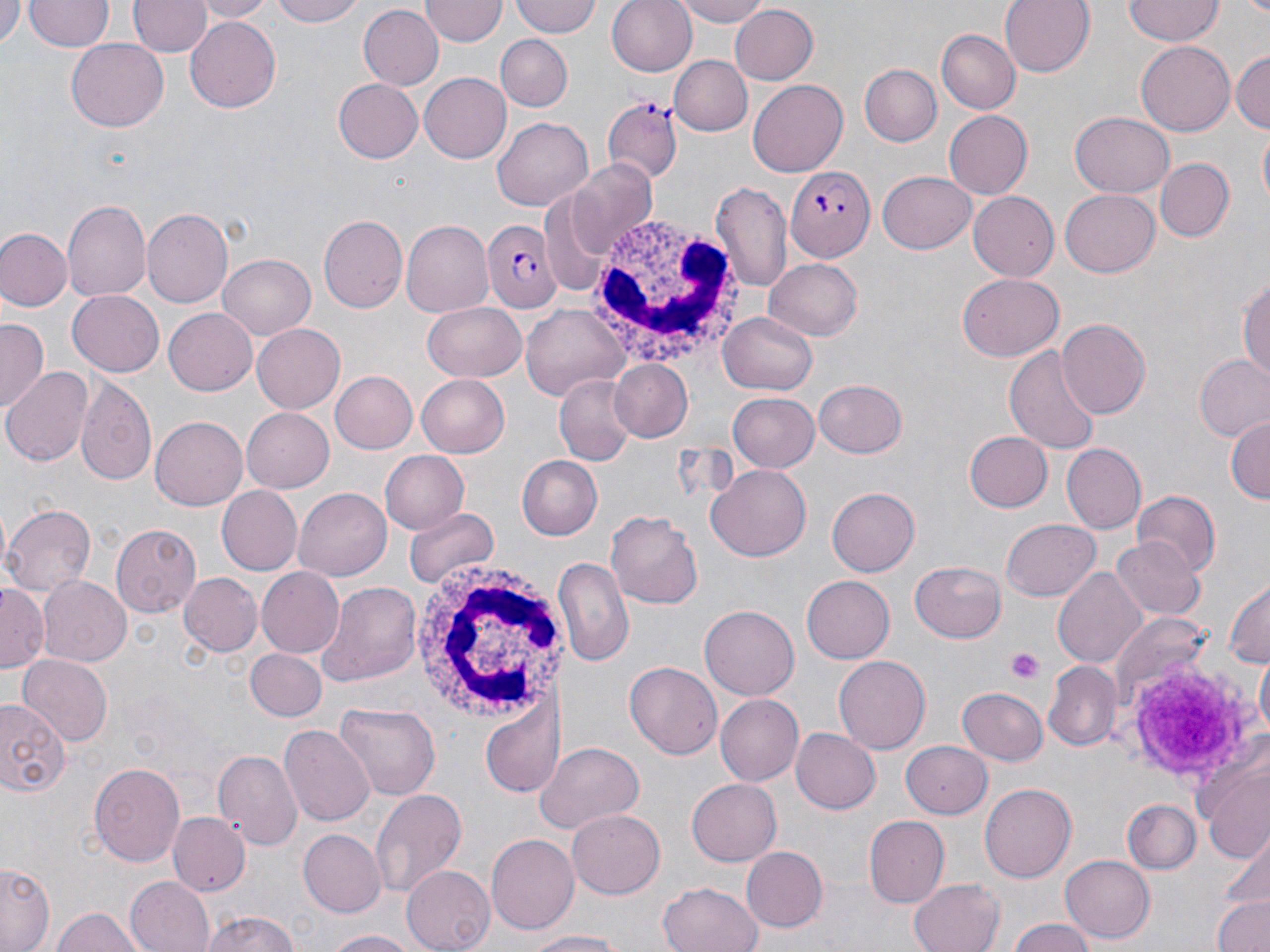 Approximate bounding boxes as [x1, y1, x2, y2] in pixels. White blood cell locations: [590, 224, 735, 364], [410, 562, 568, 724]. Platelet locations: [1005, 649, 1044, 683], [1117, 656, 1260, 788]. Uninfected red blood cell locations: [0, 0, 22, 48], [130, 0, 208, 57], [196, 0, 272, 20], [266, 0, 366, 28], [513, 0, 602, 38], [607, 0, 698, 77], [671, 0, 775, 26], [999, 0, 1095, 78], [1124, 0, 1222, 45], [25, 1, 112, 52], [422, 1, 507, 46], [359, 5, 444, 92], [727, 5, 818, 86], [186, 17, 281, 113], [935, 28, 1020, 115], [496, 34, 572, 110], [67, 39, 168, 132], [1135, 40, 1234, 135], [1231, 48, 1269, 136], [670, 55, 751, 136], [859, 64, 942, 147], [420, 73, 511, 163], [332, 79, 423, 164], [749, 80, 848, 177], [944, 110, 1032, 199], [1070, 112, 1174, 197], [495, 117, 592, 212], [1257, 128, 1270, 212], [569, 158, 659, 252], [1157, 158, 1232, 241], [879, 169, 977, 253], [714, 181, 793, 294], [1058, 190, 1161, 278], [969, 193, 1059, 282], [62, 200, 149, 304], [142, 208, 235, 308], [319, 214, 408, 314], [402, 221, 491, 315], [0, 227, 71, 310], [217, 254, 316, 339], [765, 258, 863, 340], [1238, 272, 1270, 385], [958, 273, 1062, 361], [68, 291, 163, 376], [422, 302, 527, 382], [521, 304, 631, 400], [164, 309, 258, 394], [720, 312, 819, 396], [0, 318, 49, 410], [1057, 319, 1150, 418], [251, 323, 345, 413], [1006, 343, 1102, 455], [1194, 354, 1270, 441], [609, 359, 694, 444], [3, 367, 92, 466], [329, 370, 418, 455], [416, 375, 510, 457], [552, 376, 636, 466], [77, 378, 157, 484], [814, 379, 909, 457], [727, 392, 819, 473], [241, 407, 335, 494], [1225, 414, 1270, 504], [150, 416, 247, 509], [962, 430, 1052, 512], [1060, 443, 1147, 535], [378, 451, 468, 535], [518, 455, 603, 540], [707, 464, 812, 561], [828, 485, 922, 577], [216, 486, 302, 577], [294, 487, 391, 580], [1129, 490, 1221, 576], [2, 503, 96, 598], [405, 508, 497, 590], [607, 511, 704, 609], [1002, 516, 1102, 601], [109, 522, 201, 618], [1111, 536, 1205, 621], [554, 556, 634, 669], [909, 559, 1007, 642], [1053, 565, 1150, 670], [256, 566, 345, 658], [178, 573, 263, 656], [800, 574, 894, 664], [40, 577, 129, 666], [1222, 577, 1269, 672], [315, 581, 421, 686], [0, 586, 46, 671], [700, 605, 800, 699], [1113, 611, 1212, 707], [247, 649, 326, 722], [1255, 652, 1269, 740], [16, 655, 112, 745], [833, 655, 930, 754], [625, 661, 722, 760], [1044, 661, 1119, 751], [958, 686, 1048, 765], [479, 695, 562, 797], [715, 695, 804, 786], [0, 699, 70, 800], [333, 702, 442, 801], [280, 724, 374, 827], [789, 727, 880, 814], [899, 741, 993, 818], [535, 743, 646, 833], [215, 749, 301, 849], [1195, 750, 1270, 863], [88, 761, 185, 866], [686, 777, 782, 866], [979, 783, 1075, 883], [369, 788, 469, 899], [1122, 799, 1200, 875], [567, 809, 665, 899], [169, 813, 250, 896], [865, 816, 949, 906], [297, 829, 386, 918], [485, 835, 577, 936], [741, 846, 827, 933], [1060, 855, 1155, 942], [0, 861, 54, 951], [401, 866, 494, 952], [124, 877, 214, 952], [911, 877, 1005, 952], [658, 880, 765, 952], [1212, 894, 1270, 952], [49, 906, 147, 952], [200, 910, 303, 952], [1006, 917, 1099, 952], [320, 929, 424, 952], [519, 931, 636, 951]. Plasmodium falciparum-infected red blood cell locations: [600, 99, 681, 180], [785, 165, 875, 263], [486, 219, 561, 311]. Slide-level diagnosis: Plasmodium falciparum. One field of a larger specimen. Light microscopy. May-Grünwald-Giemsa-stained preparation. Thin blood film. Image is 1270×952 pixels. 1000x magnification.